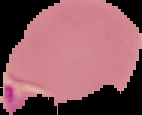
image type = segmented cell region on a black background
malaria status = parasitized
preparation = thin blood film
image size = 142×115 pixels